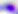 400x magnification. Photomicrograph. Toxoplasma gondii is shown.